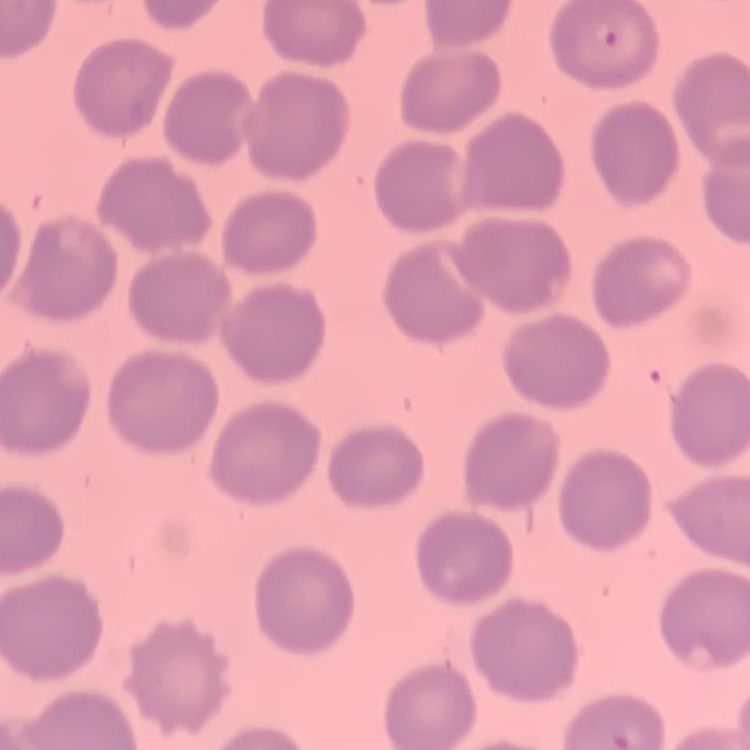
Summary:
  - Erythrocyte morphology: no rouleaux formation
  - Image type: square crop of a larger photomicrograph
  - Stain: Field's or Giemsa
  - Preparation: thin peripheral smear